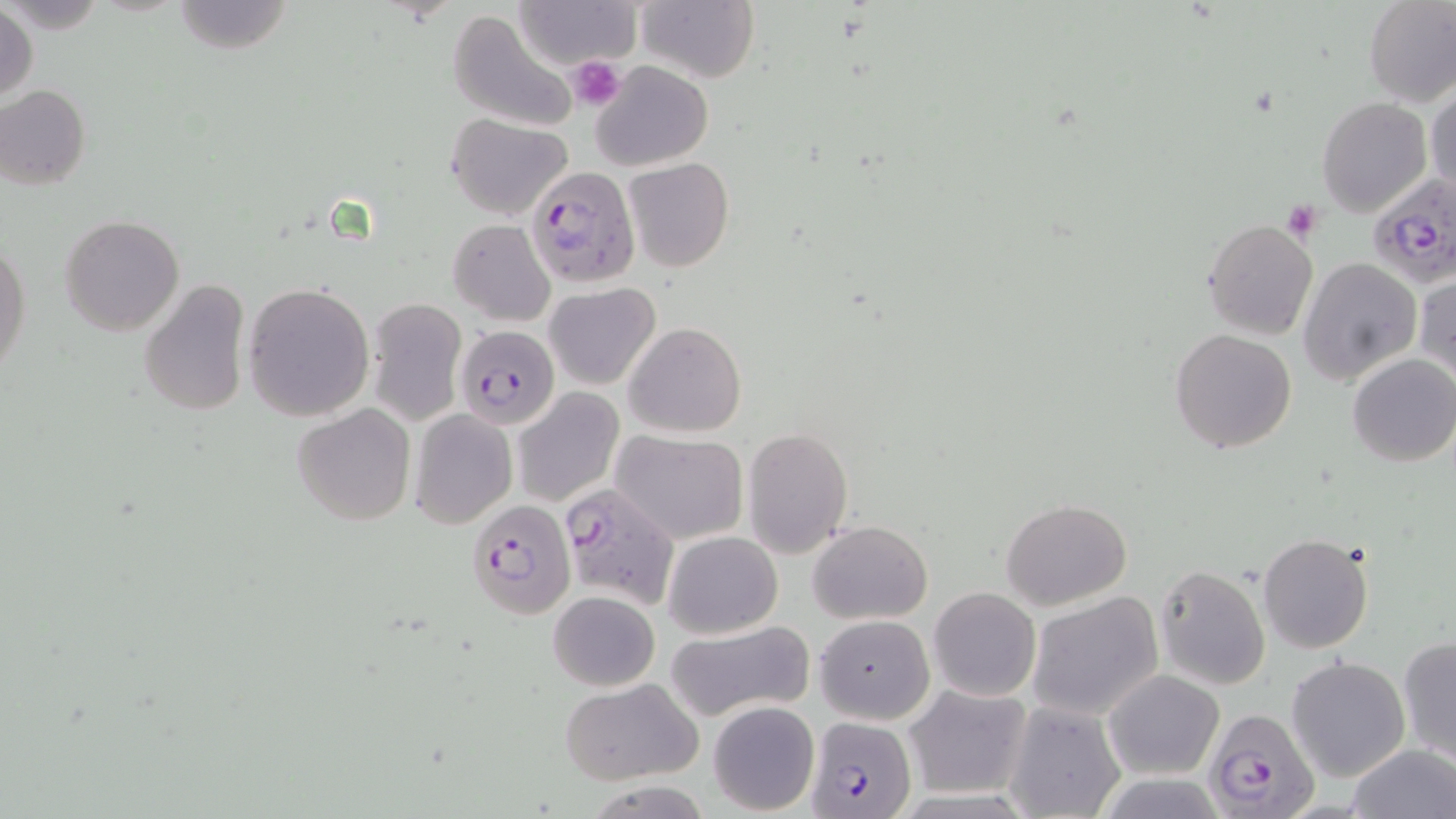

Approximate bounding boxes as named x1/y1/x2/y2 corners in pixels. Plasmodium falciparum-infected red blood cell locations: (x1=526, y1=165, x2=641, y2=288), (x1=1366, y1=175, x2=1456, y2=289), (x1=455, y1=325, x2=560, y2=429), (x1=557, y1=482, x2=681, y2=609), (x1=466, y1=499, x2=574, y2=618), (x1=1202, y1=707, x2=1318, y2=819), (x1=806, y1=717, x2=913, y2=819). Uninfected red blood cell locations: (x1=173, y1=0, x2=296, y2=55), (x1=512, y1=0, x2=643, y2=69), (x1=1362, y1=0, x2=1456, y2=108), (x1=636, y1=1, x2=758, y2=83), (x1=0, y1=3, x2=38, y2=105), (x1=448, y1=9, x2=580, y2=132), (x1=589, y1=60, x2=713, y2=170), (x1=0, y1=84, x2=89, y2=189), (x1=1427, y1=84, x2=1455, y2=200), (x1=1317, y1=98, x2=1433, y2=218), (x1=445, y1=112, x2=574, y2=220), (x1=623, y1=156, x2=734, y2=272), (x1=61, y1=214, x2=184, y2=336), (x1=448, y1=220, x2=556, y2=325), (x1=1202, y1=220, x2=1317, y2=340), (x1=1, y1=237, x2=31, y2=381), (x1=1298, y1=258, x2=1421, y2=387), (x1=1414, y1=270, x2=1456, y2=386), (x1=138, y1=280, x2=251, y2=419), (x1=242, y1=281, x2=374, y2=420), (x1=544, y1=284, x2=660, y2=389), (x1=365, y1=298, x2=469, y2=426), (x1=623, y1=322, x2=747, y2=438), (x1=1170, y1=328, x2=1297, y2=453), (x1=1347, y1=353, x2=1456, y2=467), (x1=513, y1=388, x2=623, y2=505), (x1=292, y1=403, x2=416, y2=528), (x1=409, y1=409, x2=517, y2=527), (x1=742, y1=426, x2=853, y2=558), (x1=612, y1=429, x2=748, y2=543), (x1=1000, y1=497, x2=1132, y2=607), (x1=808, y1=521, x2=933, y2=625), (x1=664, y1=531, x2=783, y2=638), (x1=1258, y1=533, x2=1376, y2=654), (x1=1153, y1=563, x2=1270, y2=691), (x1=927, y1=587, x2=1041, y2=702), (x1=548, y1=590, x2=660, y2=692), (x1=1028, y1=591, x2=1166, y2=722), (x1=815, y1=615, x2=935, y2=724), (x1=665, y1=619, x2=815, y2=724), (x1=1398, y1=636, x2=1456, y2=762), (x1=1286, y1=656, x2=1410, y2=781), (x1=1103, y1=669, x2=1223, y2=779), (x1=558, y1=678, x2=702, y2=785), (x1=903, y1=684, x2=1031, y2=798), (x1=1005, y1=700, x2=1125, y2=818), (x1=707, y1=701, x2=820, y2=815), (x1=1344, y1=744, x2=1455, y2=819). Platelet locations: (x1=567, y1=55, x2=625, y2=109), (x1=1280, y1=203, x2=1322, y2=242). Slide-level diagnosis: Plasmodium falciparum. 1000x magnification. May-Grünwald-Giemsa stain. One field of a larger specimen. Optical microscopy. Thin blood smear. Image is 1456×819 pixels.